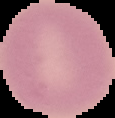
result: negative for malaria parasites
preparation: thin blood smear
image_type: segmented cell region with the area outside set to black
image_size: 115×118 pixels